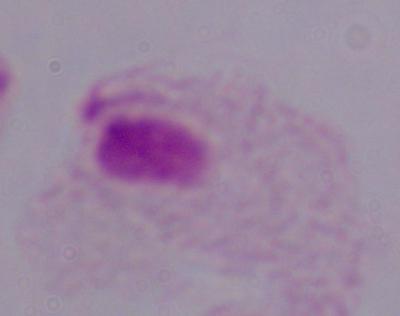
Photomicrograph. 1000x magnification. A trichomonad is seen.